Assess this cell for malaria.
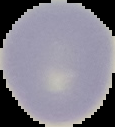

Uninfected.

{
  "image_size": "115×127 pixels",
  "image_type": "cell region segmented out of the field of view; surrounding area masked to black",
  "preparation": "thin blood film"
}